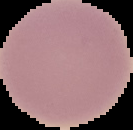 From a thin blood film. Image is 133×130 pixels. Cell region segmented out of the field of view; the surrounding area is masked to black. Result: no Plasmodium parasites detected.